Locate and identify every blood parasite.
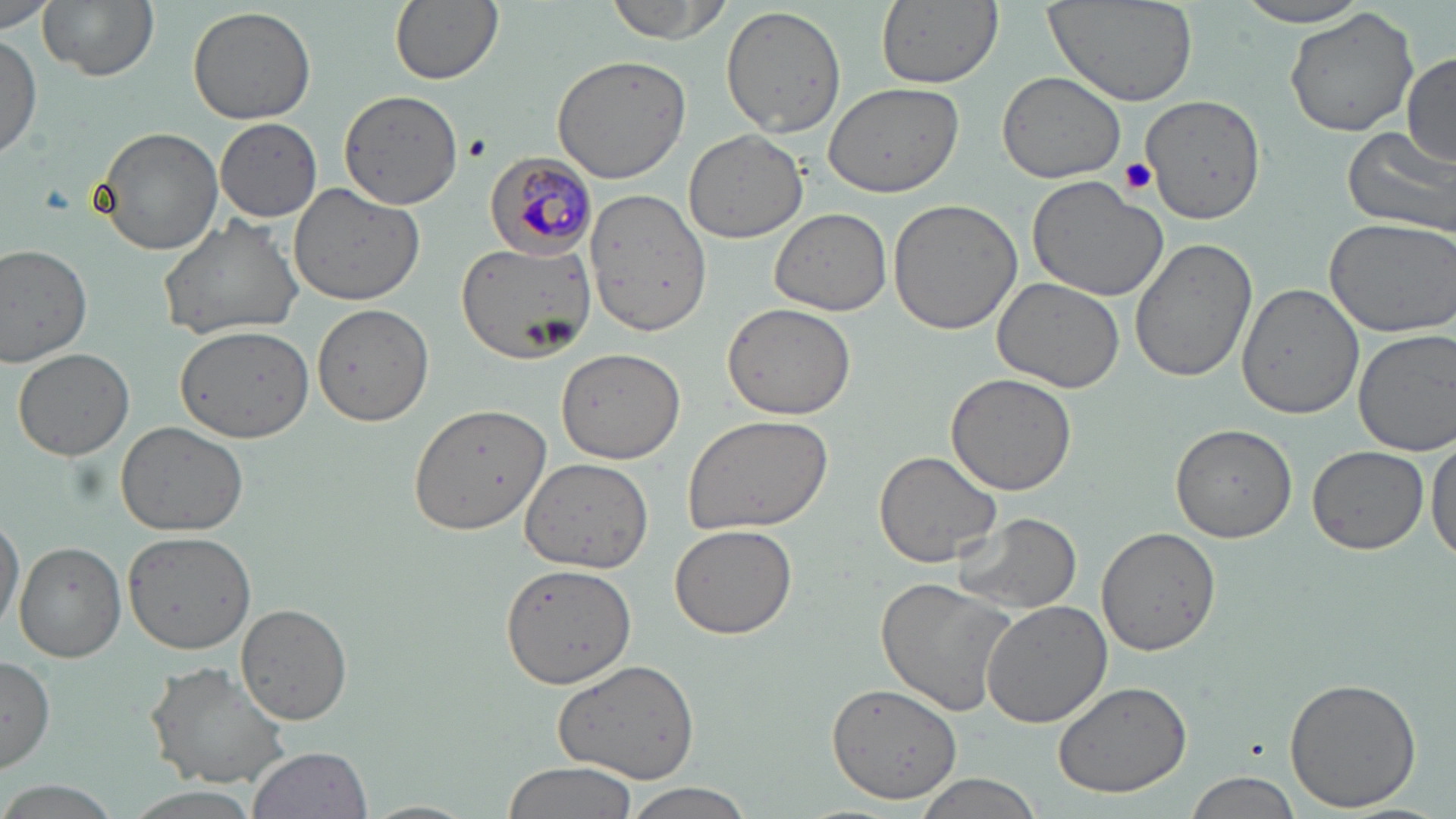
Approximate bounding boxes as named x1/y1/x2/y2 corners in pixels.
Plasmodium malariae-infected red blood cells: (x1=485, y1=152, x2=598, y2=259).
No Plasmodium falciparum, Plasmodium ovale, Plasmodium vivax, Babesia divergens, or Trypanosoma brucei observed.

Platelet locations: (x1=462, y1=134, x2=492, y2=162), (x1=1116, y1=158, x2=1156, y2=198). Uninfected red blood cell locations: (x1=38, y1=0, x2=160, y2=82), (x1=389, y1=0, x2=503, y2=86), (x1=605, y1=0, x2=733, y2=43), (x1=875, y1=0, x2=1004, y2=88), (x1=1041, y1=0, x2=1200, y2=108), (x1=1, y1=1, x2=61, y2=35), (x1=1232, y1=1, x2=1377, y2=28), (x1=720, y1=4, x2=847, y2=139), (x1=187, y1=5, x2=318, y2=124), (x1=1284, y1=6, x2=1424, y2=139), (x1=0, y1=33, x2=43, y2=161), (x1=551, y1=53, x2=695, y2=184), (x1=1401, y1=53, x2=1456, y2=165), (x1=997, y1=71, x2=1127, y2=183), (x1=823, y1=82, x2=964, y2=199), (x1=337, y1=88, x2=464, y2=211), (x1=1141, y1=95, x2=1266, y2=224), (x1=214, y1=118, x2=324, y2=222), (x1=94, y1=127, x2=223, y2=255), (x1=1342, y1=127, x2=1456, y2=238), (x1=684, y1=129, x2=809, y2=243), (x1=1027, y1=173, x2=1170, y2=302), (x1=288, y1=180, x2=430, y2=304), (x1=584, y1=185, x2=712, y2=336), (x1=887, y1=199, x2=1023, y2=335), (x1=769, y1=208, x2=892, y2=316), (x1=156, y1=213, x2=305, y2=339), (x1=1322, y1=216, x2=1456, y2=337), (x1=1129, y1=239, x2=1258, y2=383), (x1=455, y1=241, x2=596, y2=362), (x1=0, y1=245, x2=93, y2=367), (x1=991, y1=277, x2=1124, y2=393), (x1=1238, y1=281, x2=1363, y2=418), (x1=310, y1=301, x2=436, y2=429), (x1=723, y1=303, x2=856, y2=421), (x1=176, y1=324, x2=314, y2=441), (x1=1353, y1=326, x2=1456, y2=457), (x1=13, y1=347, x2=134, y2=461), (x1=556, y1=348, x2=685, y2=464), (x1=946, y1=373, x2=1077, y2=496), (x1=409, y1=402, x2=551, y2=535), (x1=681, y1=413, x2=835, y2=536), (x1=114, y1=421, x2=249, y2=535), (x1=1170, y1=423, x2=1297, y2=543), (x1=1428, y1=434, x2=1456, y2=564), (x1=1307, y1=445, x2=1429, y2=555), (x1=874, y1=449, x2=1003, y2=567), (x1=518, y1=456, x2=655, y2=573), (x1=0, y1=511, x2=23, y2=637), (x1=951, y1=511, x2=1084, y2=617), (x1=671, y1=524, x2=798, y2=640), (x1=1096, y1=526, x2=1221, y2=656), (x1=122, y1=529, x2=258, y2=654), (x1=15, y1=540, x2=126, y2=662), (x1=500, y1=562, x2=636, y2=688), (x1=875, y1=578, x2=1020, y2=718), (x1=980, y1=599, x2=1114, y2=729), (x1=235, y1=604, x2=352, y2=725), (x1=0, y1=653, x2=55, y2=775), (x1=551, y1=657, x2=703, y2=789), (x1=145, y1=663, x2=293, y2=790), (x1=1284, y1=674, x2=1424, y2=813), (x1=1051, y1=679, x2=1194, y2=798), (x1=827, y1=681, x2=963, y2=805), (x1=247, y1=746, x2=372, y2=819), (x1=503, y1=760, x2=636, y2=819), (x1=1184, y1=770, x2=1300, y2=819), (x1=910, y1=774, x2=1045, y2=818), (x1=617, y1=781, x2=760, y2=819), (x1=3, y1=782, x2=118, y2=819), (x1=121, y1=787, x2=267, y2=819), (x1=362, y1=798, x2=480, y2=819). Slide-level diagnosis: Plasmodium malariae. Optical microscopy. Image is 1456×819 pixels. 1000x magnification. One field of a larger specimen. May-Grünwald-Giemsa stain. Thin blood film.